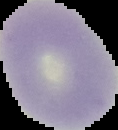

Summary:
  - Preparation: thin blood smear
  - Result: negative for malaria parasites
  - Image size: 118×130 pixels
  - Image type: segmented cell region with the area outside set to black